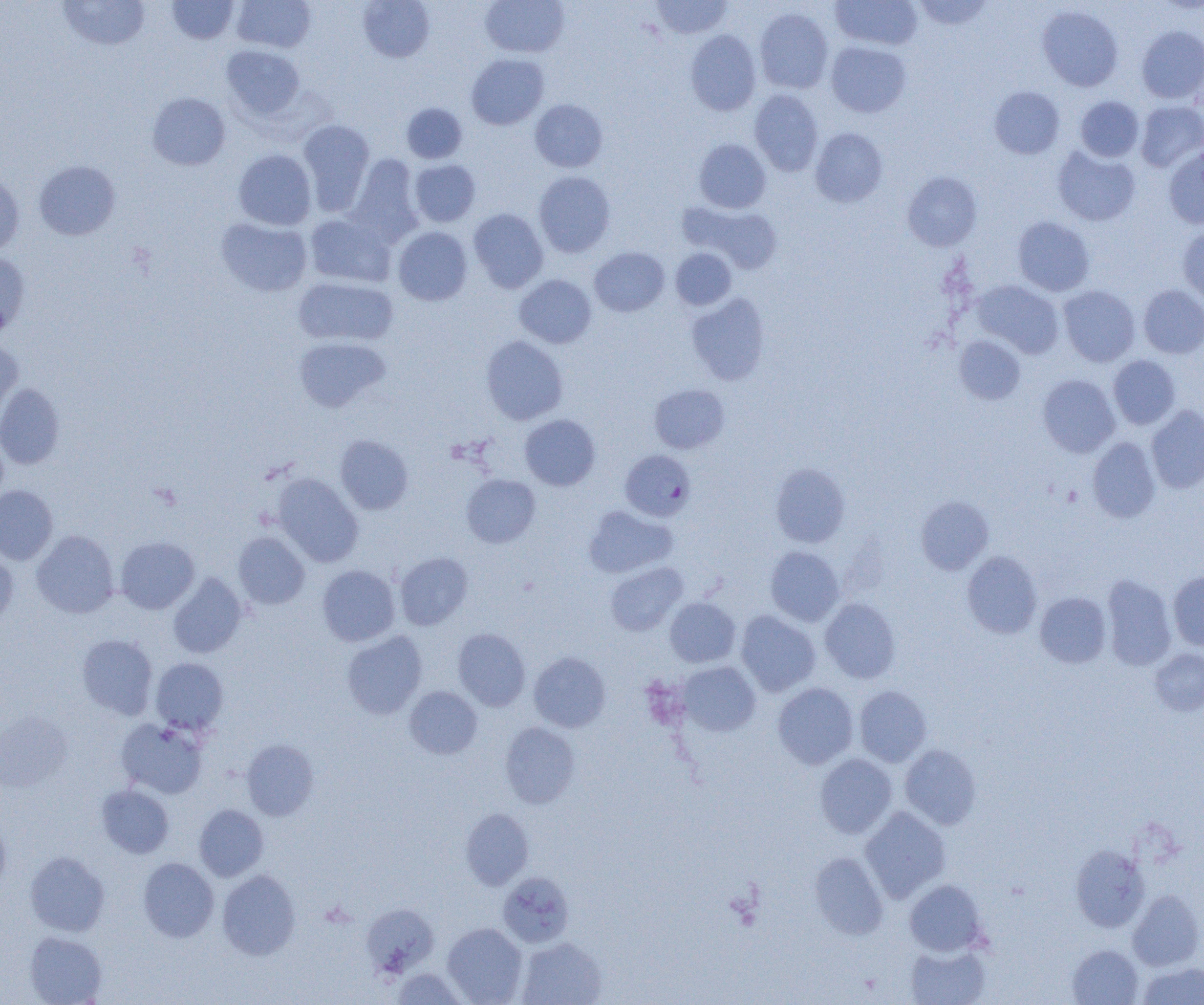
Summary:
  - Coordinate format: approximate bounding boxes as (x1, y1, x2, y2) in pixels
  - Plasmodium falciparum-infected red blood cell locations: (620, 450, 695, 521)
  - Uninfected red blood cell locations: (58, 0, 150, 51), (167, 0, 239, 44), (232, 0, 316, 52), (358, 0, 435, 62), (480, 0, 570, 57), (651, 0, 732, 39), (832, 0, 922, 50), (914, 0, 993, 30), (1037, 5, 1123, 91), (755, 8, 833, 93), (1137, 26, 1204, 104), (686, 30, 761, 116), (826, 41, 911, 117), (221, 45, 305, 120), (466, 54, 548, 129), (989, 86, 1064, 159), (749, 90, 823, 175), (147, 92, 230, 170), (1076, 96, 1144, 161), (530, 99, 608, 172), (1135, 101, 1204, 172), (402, 103, 467, 163), (297, 119, 375, 215), (810, 128, 888, 207), (694, 139, 770, 213), (1052, 147, 1140, 226), (1164, 147, 1204, 229), (233, 149, 316, 230), (347, 154, 424, 246), (409, 159, 480, 227), (34, 161, 120, 240), (533, 171, 616, 257), (902, 171, 982, 251), (0, 172, 24, 254), (681, 202, 783, 274), (469, 208, 548, 293), (305, 213, 395, 287), (1012, 216, 1094, 296), (216, 218, 312, 297), (1177, 226, 1204, 305), (393, 227, 472, 305), (590, 247, 669, 316), (670, 248, 736, 310), (0, 252, 31, 335), (514, 274, 597, 348), (293, 276, 398, 346), (973, 280, 1063, 358), (1138, 285, 1204, 358), (1058, 286, 1139, 366), (686, 293, 771, 385), (481, 335, 568, 425), (293, 336, 390, 412), (955, 336, 1026, 404), (0, 339, 23, 421), (1108, 355, 1180, 429), (1037, 375, 1119, 457), (0, 383, 65, 469), (649, 384, 729, 453), (1146, 405, 1204, 493), (520, 414, 600, 490), (335, 435, 414, 515), (1087, 437, 1161, 523), (770, 464, 850, 547), (272, 473, 363, 567), (462, 474, 540, 548), (0, 485, 58, 565), (916, 496, 994, 574), (583, 506, 677, 578), (31, 530, 119, 618), (233, 532, 310, 609), (115, 536, 199, 614), (765, 546, 844, 626), (0, 549, 18, 629), (962, 550, 1042, 638), (395, 552, 473, 630), (605, 562, 687, 636), (317, 565, 400, 646), (1168, 571, 1204, 651), (168, 573, 247, 658), (1102, 574, 1176, 671), (1035, 592, 1111, 668), (665, 597, 740, 667), (820, 598, 900, 683), (736, 610, 820, 696), (453, 628, 530, 711), (342, 631, 427, 719), (77, 634, 157, 719), (1150, 648, 1204, 716), (529, 652, 610, 732), (151, 657, 228, 735), (678, 662, 760, 736), (773, 683, 858, 768), (854, 685, 932, 766), (405, 686, 482, 759), (1, 711, 71, 793), (116, 718, 207, 799), (500, 722, 580, 809), (241, 739, 319, 820), (900, 744, 982, 829), (815, 754, 897, 838), (97, 784, 174, 858), (194, 804, 269, 881), (860, 807, 951, 902), (460, 808, 533, 889), (0, 818, 11, 894), (1070, 844, 1149, 932), (25, 851, 110, 937), (810, 852, 888, 939), (138, 857, 218, 942), (217, 870, 301, 960), (498, 871, 575, 947), (905, 879, 987, 956), (1128, 890, 1203, 970), (361, 903, 439, 976), (442, 923, 527, 1004), (25, 931, 107, 1004), (516, 937, 607, 1005), (905, 942, 991, 1005), (1067, 945, 1143, 1005), (1137, 962, 1204, 1005), (393, 969, 467, 1005)
  - Slide-level diagnosis: Plasmodium falciparum
  - Field of view: single
  - Image size: 1204×1005 pixels
  - Magnification: 1000x
  - Modality: optical microscopy
  - Preparation: thin blood film